Point out each leukocyte.
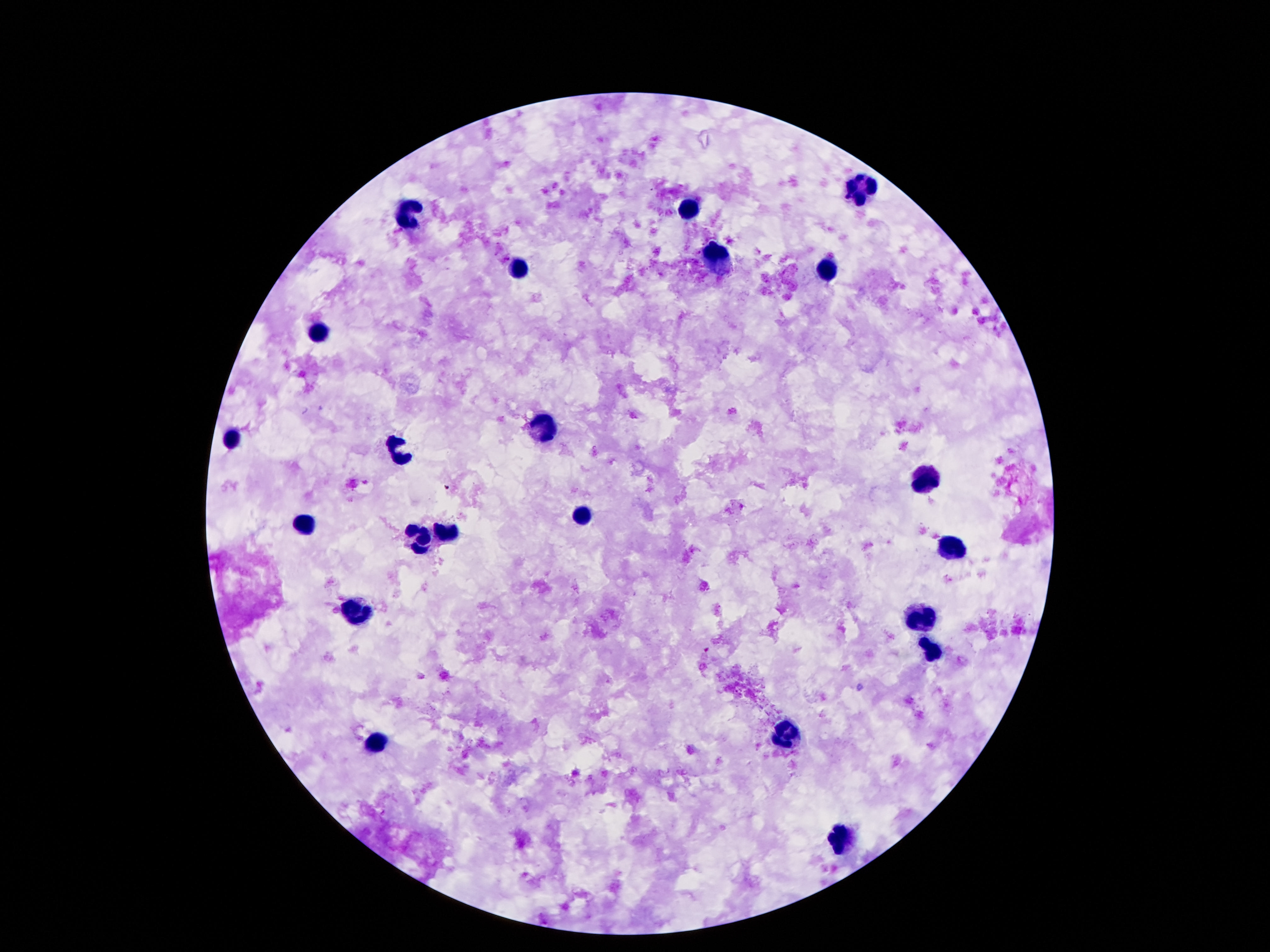

Approximate centers as {x, y} in pixels.
Leukocytes: {857, 188}, {412, 209}, {687, 209}, {719, 267}, {523, 269}, {826, 271}, {324, 331}, {544, 424}, {229, 439}, {399, 454}, {922, 477}, {582, 515}, {298, 525}, {441, 536}, {414, 540}, {952, 547}, {922, 615}, {353, 617}, {931, 651}, {792, 734}, {374, 744}, {840, 837}.

Giemsa stain. 100x magnification. Patient malaria status: negative. Thick blood film. Smartphone photograph taken through the microscope eyepiece. Single field of view. Image is 1270×952 pixels.